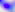
400x magnification. Toxoplasma gondii is shown. Photomicrograph.